Classify this cell by malaria status.
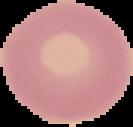
Uninfected.

Summary:
  - Preparation: thin blood film
  - Image type: segmented cell region with the area outside set to black
  - Image size: 133×127 pixels